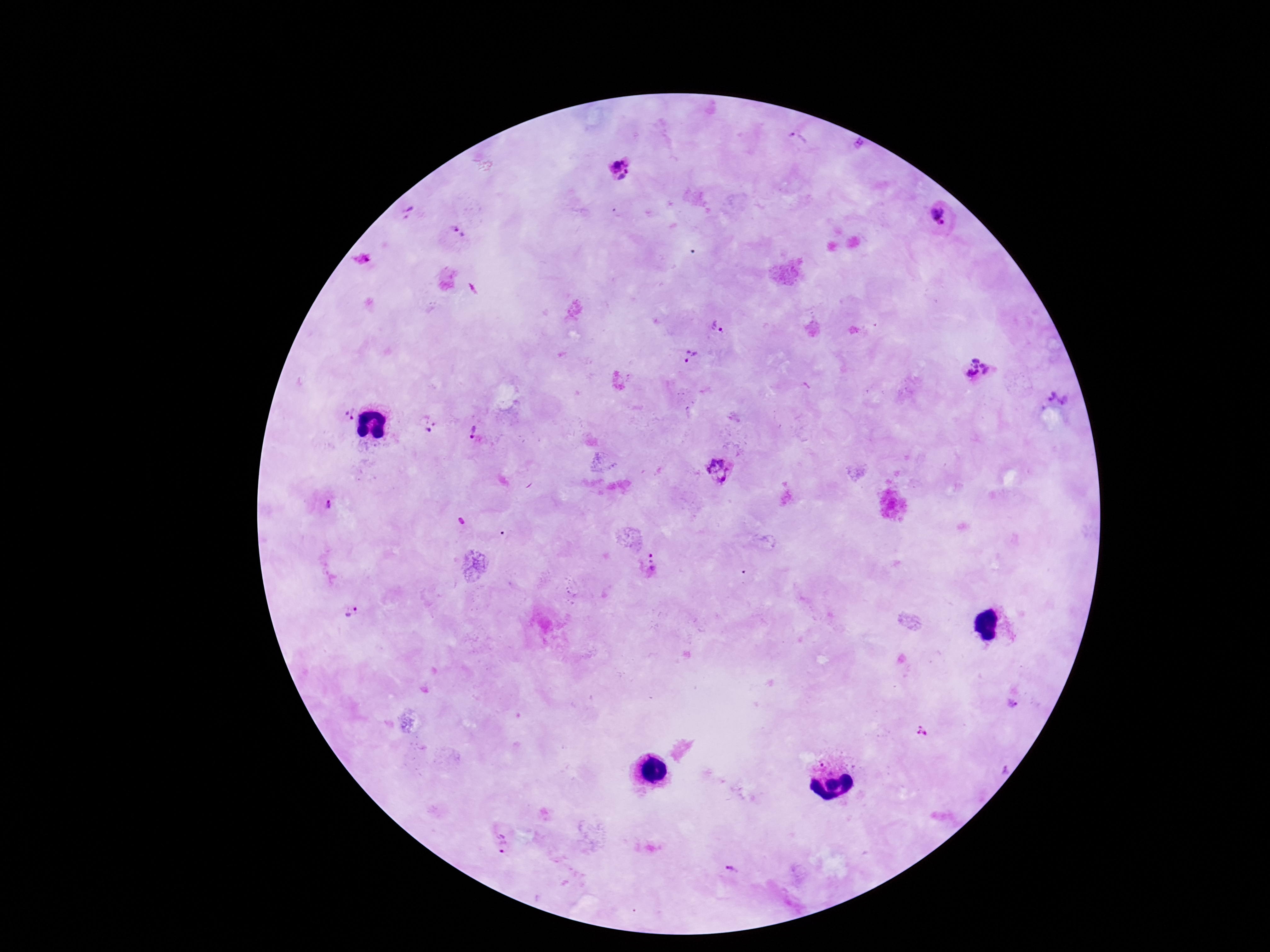

field of view = one from this slide
magnification = 100x
preparation = thick blood film
patient malaria status = infected
Plasmodium parasite locations = approximate centers as [x, y] in pixels: [797, 139], [862, 144], [621, 168], [407, 215], [940, 219], [456, 232], [361, 260], [718, 328], [692, 358], [979, 368], [1055, 400], [348, 411], [430, 426], [472, 433], [719, 472], [328, 503], [652, 566], [348, 611], [1009, 701], [922, 732], [1002, 770], [499, 842], [734, 872]
capture = smartphone camera through the microscope eyepiece
image size = 1270×952 pixels
stain = Giemsa